Classify this cell by malaria status.
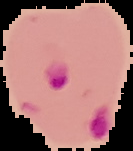
It is parasitized.

From a thin blood film. The area outside the segmented cell region is set to black. Image is 133×151 pixels.